State which cell type is depicted.
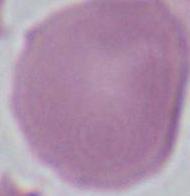
An erythrocyte.

modality = photomicrograph
magnification = 1000x